Give the extent of all uninfected red blood cells.
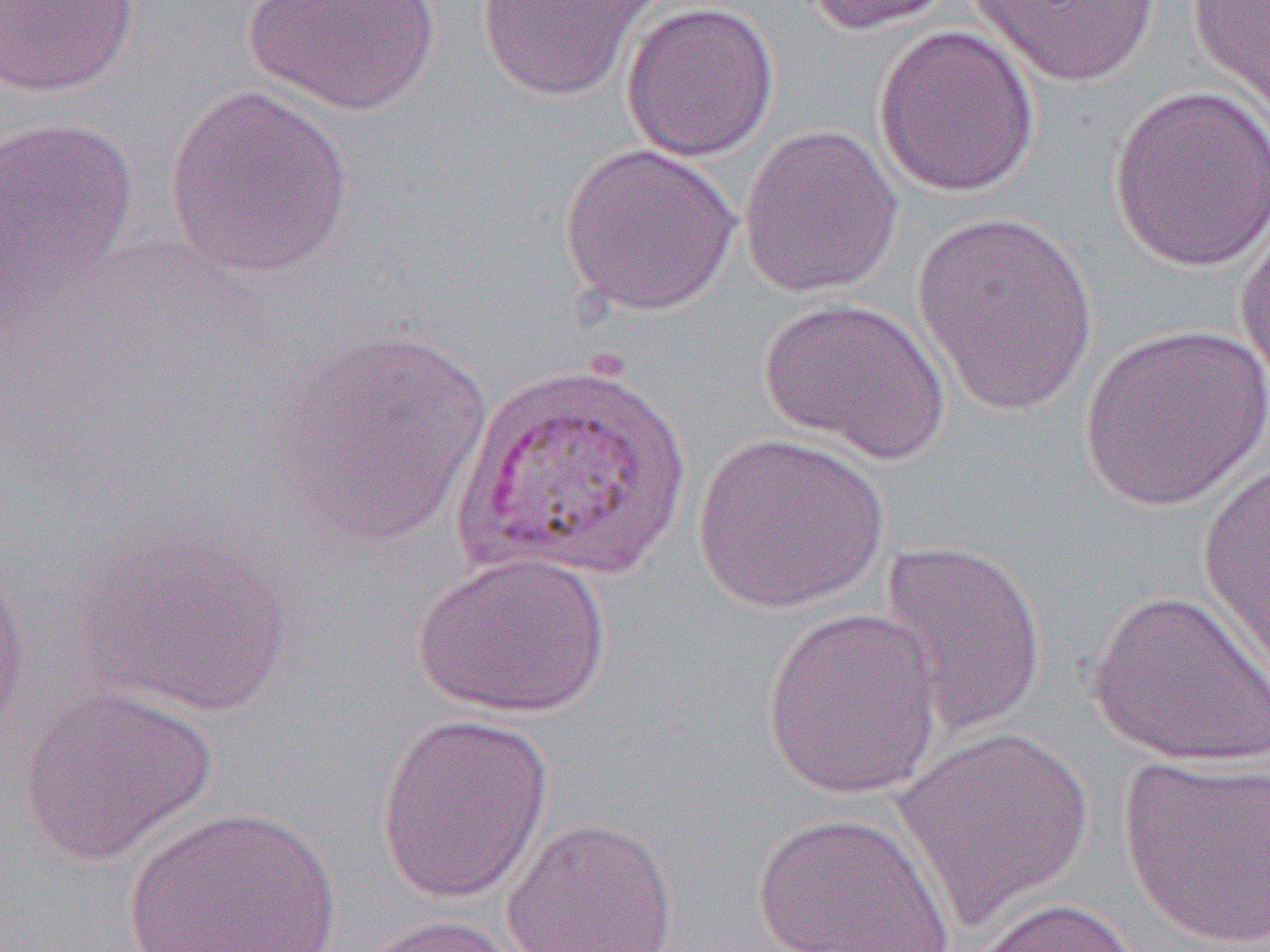

Approximate bounding boxes as (x1, y1, x2, y2) in pixels.
Uninfected red blood cells: (241, 0, 445, 115), (474, 0, 664, 102), (802, 0, 957, 36), (969, 0, 1160, 86), (1187, 0, 1270, 127), (1, 1, 139, 97), (620, 1, 780, 162), (872, 24, 1041, 198), (164, 84, 356, 280), (1107, 84, 1270, 273), (0, 114, 139, 307), (738, 124, 904, 299), (560, 142, 743, 316), (910, 210, 1100, 415), (1234, 212, 1270, 392), (758, 295, 953, 465), (1077, 322, 1270, 512), (274, 328, 494, 549), (692, 431, 890, 614), (1197, 454, 1270, 685), (77, 525, 294, 719), (877, 538, 1049, 738), (0, 545, 32, 744), (412, 551, 613, 720), (1088, 588, 1270, 768), (760, 606, 946, 801), (19, 687, 218, 866), (375, 711, 555, 905), (894, 724, 1095, 925), (1116, 754, 1270, 949), (121, 805, 344, 951), (752, 811, 956, 952), (501, 816, 679, 952), (963, 896, 1149, 952), (352, 913, 528, 952).

Slide-level diagnosis: Plasmodium vivax. Optical microscopy. Image is 1270×952 pixels. Single field of view. Captured at 1000x magnification. Thin blood smear.